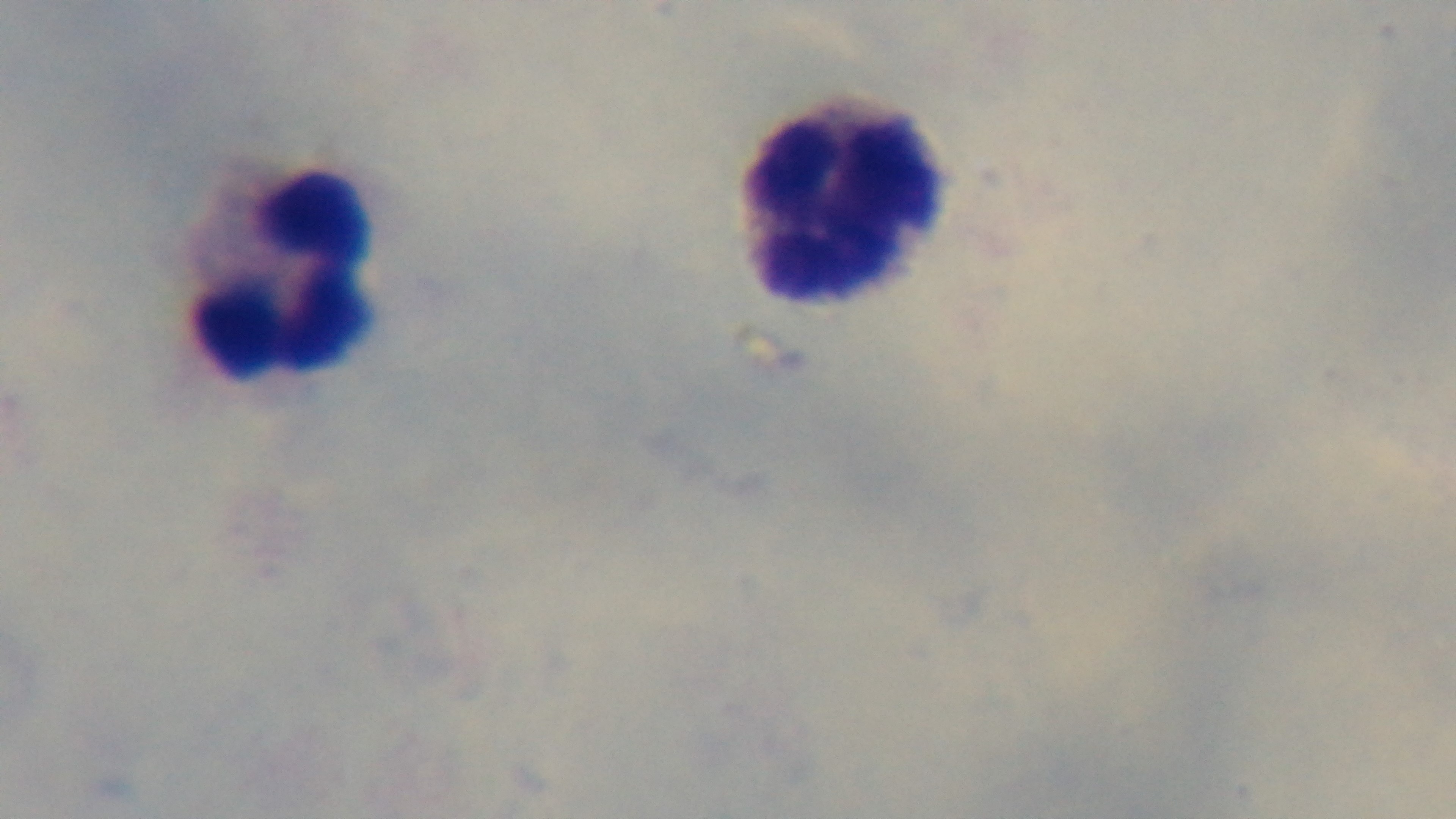 Light microscopy. Mounted 4K digital camera. Oil-immersion objective, 100x. Malaria status: uninfected. Single field of view. Preparation: thick. Giemsa-stained.